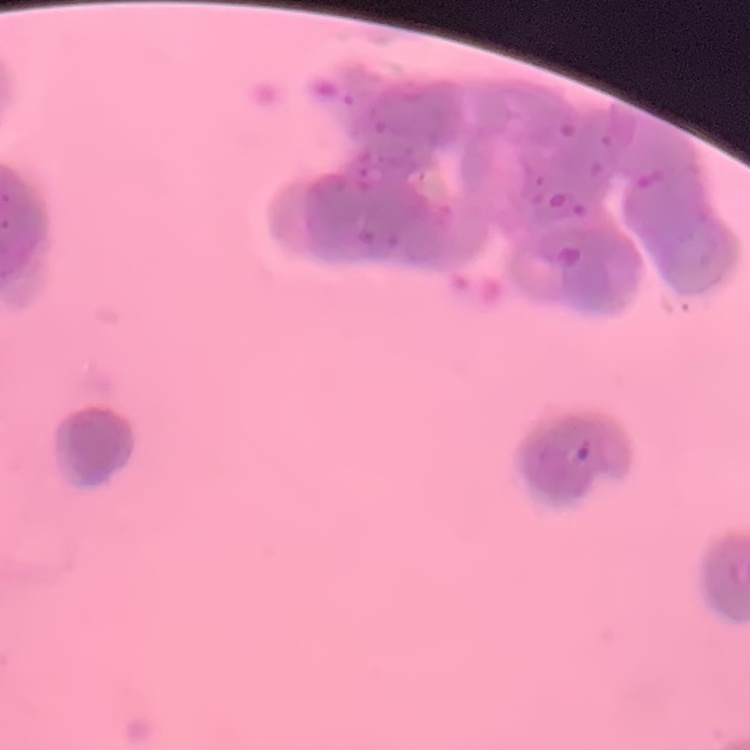
Summary:
  - Erythrocyte morphology: rouleaux formation
  - Preparation: thin blood smear
  - Image type: square crop of a larger photomicrograph
  - Stain: Field's or Giemsa